Locate every leukocyte (white blood cell).
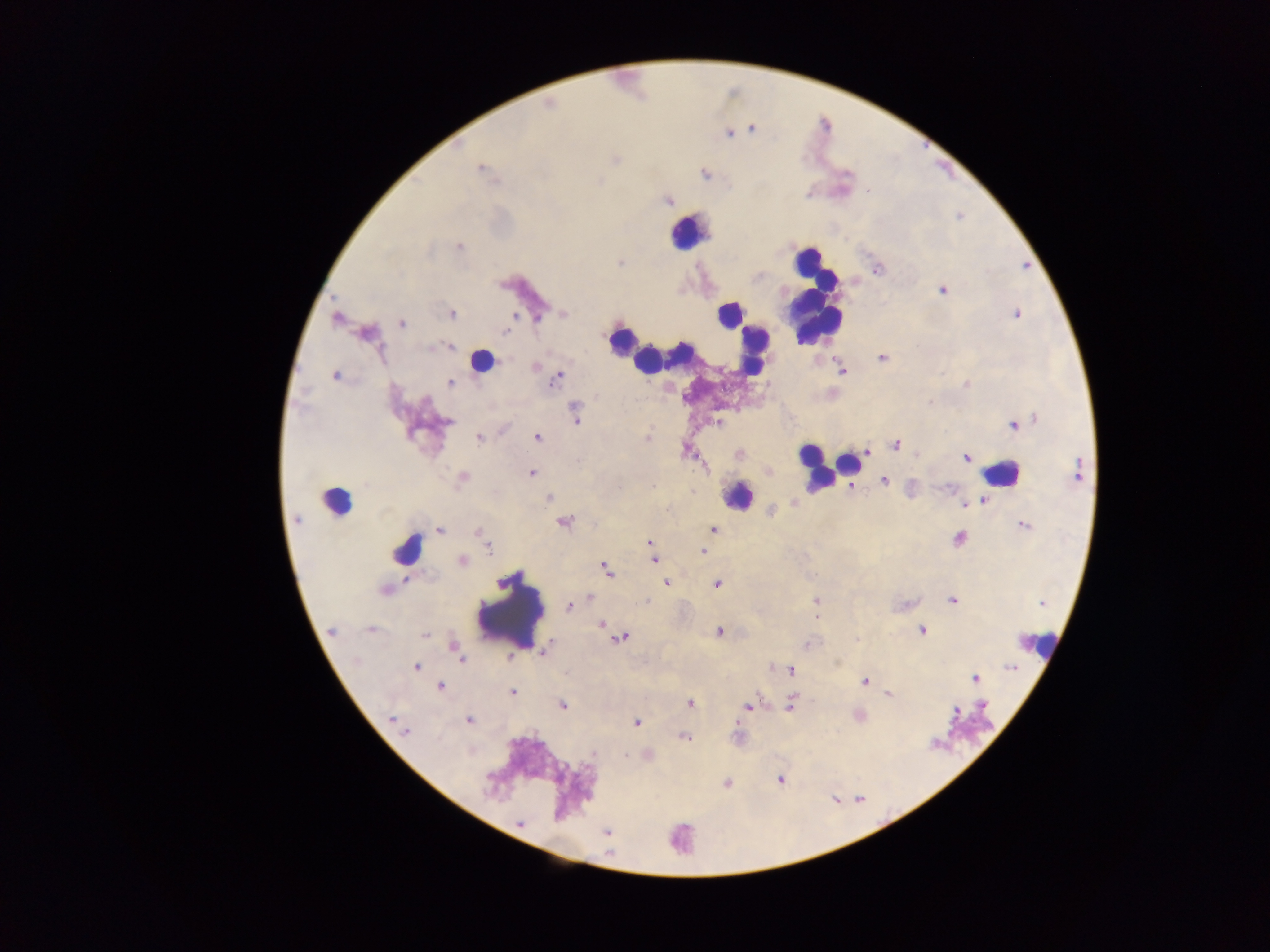

Approximate centers as [x, y] in pixels.
Leukocytes: [689, 232], [816, 301], [729, 315], [620, 338], [639, 347], [753, 349], [666, 357], [648, 360], [482, 361], [849, 463], [816, 466], [1001, 474], [738, 496], [336, 502], [407, 548], [510, 613], [1038, 645], [972, 726], [680, 838].

Plasmodium parasite locations: [549, 103], [751, 129], [728, 133], [480, 169], [705, 174], [668, 200], [459, 246], [620, 263], [876, 269], [942, 290], [451, 313], [562, 313], [1016, 313], [336, 317], [401, 323], [506, 330], [367, 333], [448, 346], [882, 358], [536, 367], [840, 369], [335, 375], [558, 375], [450, 383], [966, 384], [576, 414], [446, 422], [718, 422], [1012, 423], [537, 437], [479, 438], [647, 438], [895, 444], [685, 449], [872, 449], [866, 450], [739, 454], [965, 457], [767, 470], [1077, 470], [531, 473], [462, 478], [884, 480], [851, 487], [549, 498], [982, 501], [793, 503], [963, 503], [772, 510], [296, 520], [564, 522], [1024, 525], [713, 529], [440, 530], [480, 532], [959, 537], [485, 539], [649, 543], [487, 546], [701, 550], [654, 559], [462, 561], [606, 569], [666, 582], [716, 584], [384, 590], [589, 598], [952, 599], [816, 601], [1042, 603], [570, 605], [816, 616], [601, 624], [331, 630], [371, 630], [921, 630], [719, 631], [425, 634], [621, 637], [454, 647], [545, 649], [510, 657], [460, 660], [416, 666], [1010, 667], [791, 669], [974, 677], [865, 681], [441, 686], [512, 692], [888, 693], [690, 703], [790, 703], [562, 704], [748, 707], [469, 719], [396, 722], [635, 722], [402, 729], [683, 737], [647, 755], [780, 779], [726, 783], [520, 823], [606, 832]. Image is 1270×952 pixels. Single field of view. Mobile-phone photograph taken through the microscope. Collected in Ghana. Thick blood smear.